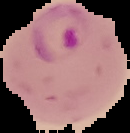

image_size: 130×133 pixels
result: Plasmodium parasites detected
preparation: thin blood film
image_type: segmented cell region with the area outside set to black